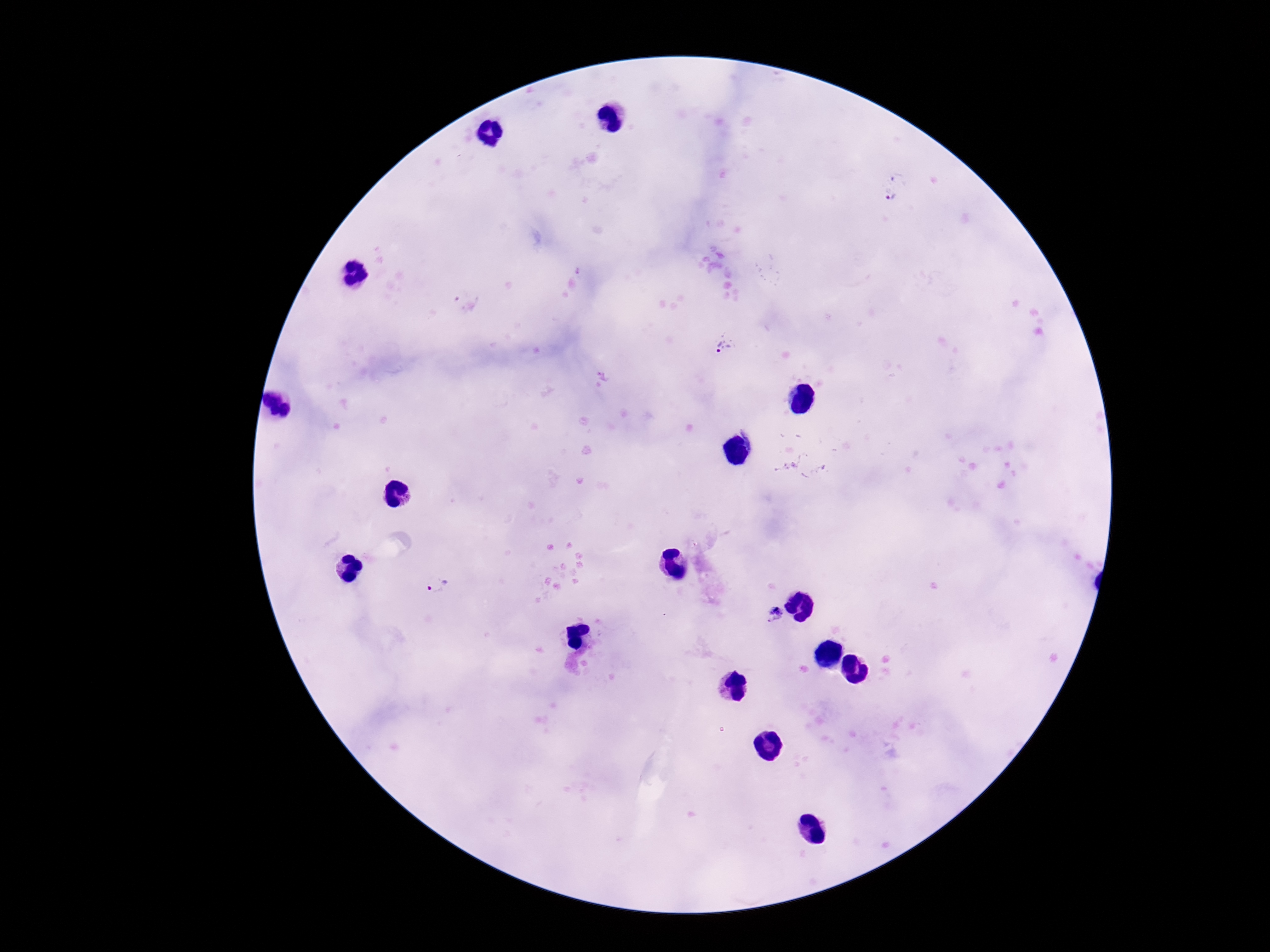 Approximate object centers, in pixels from the top-left corner. Plasmodium parasite locations: (x=895, y=199), (x=724, y=345), (x=437, y=586), (x=775, y=615). Image is 1270×952 pixels. 100x magnification. One field from this slide. Patient malaria status: infected. Thick blood film. Photographed through the microscope eyepiece with a smartphone camera. Giemsa stain.